Look for Plasmodium parasites.
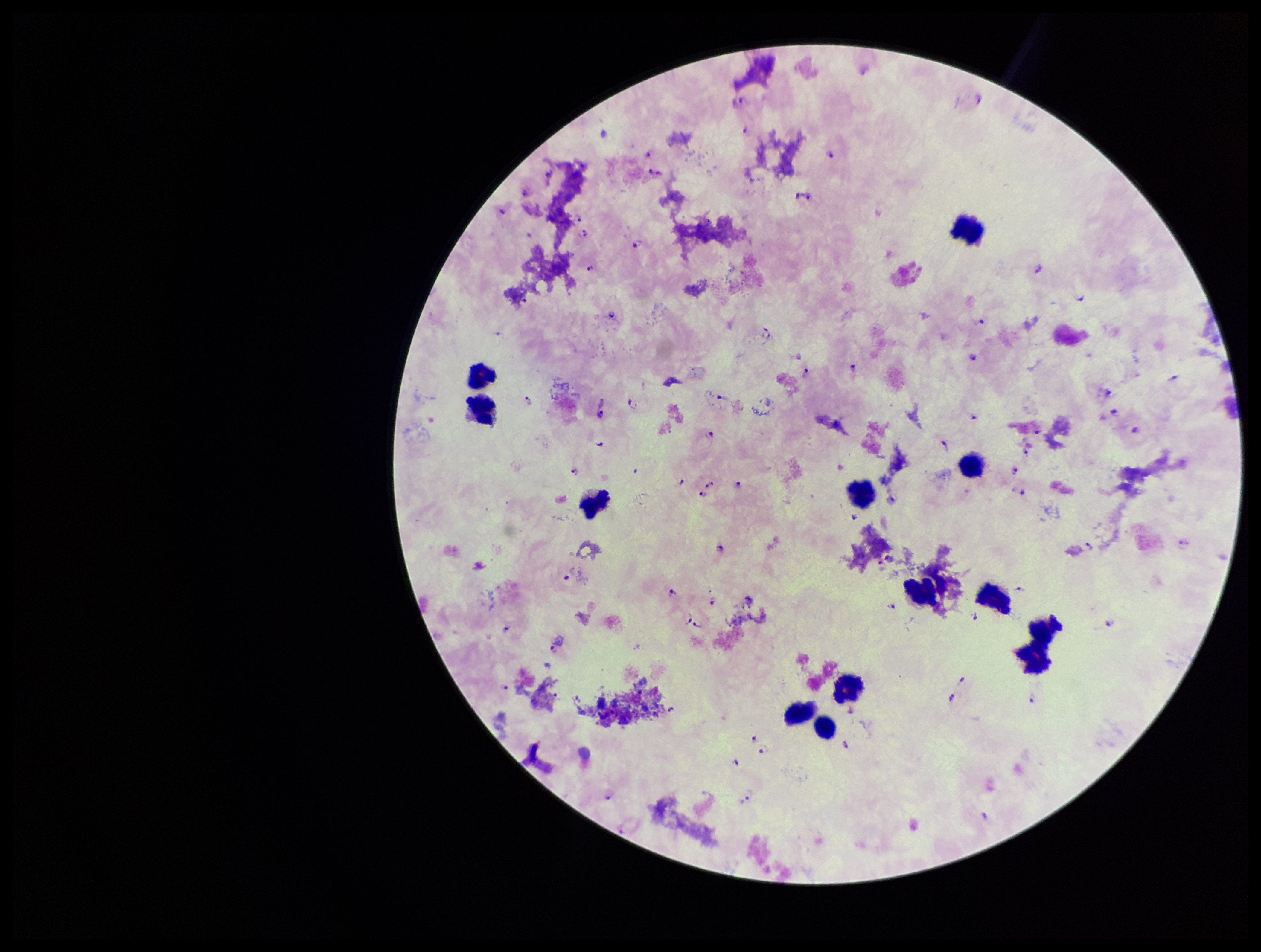
Identified.

Patient malaria status: infected. Stained with Giemsa. Photographed through the microscope eyepiece with a smartphone camera. Species reported for this patient: Plasmodium falciparum. Parasite count: 85. Leukocyte count: 13. Image is 1261×952 pixels. Preparation: thick. One field from this slide.